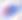

Summary:
  - Modality: photomicrograph
  - Identification: Toxoplasma gondii
  - Magnification: 400x